Report the malaria status of this cell.
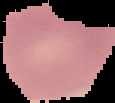
It is uninfected.

Summary:
  - Image type: cell region segmented out of the field of view; surrounding area masked to black
  - Preparation: thin blood film
  - Image size: 115×103 pixels